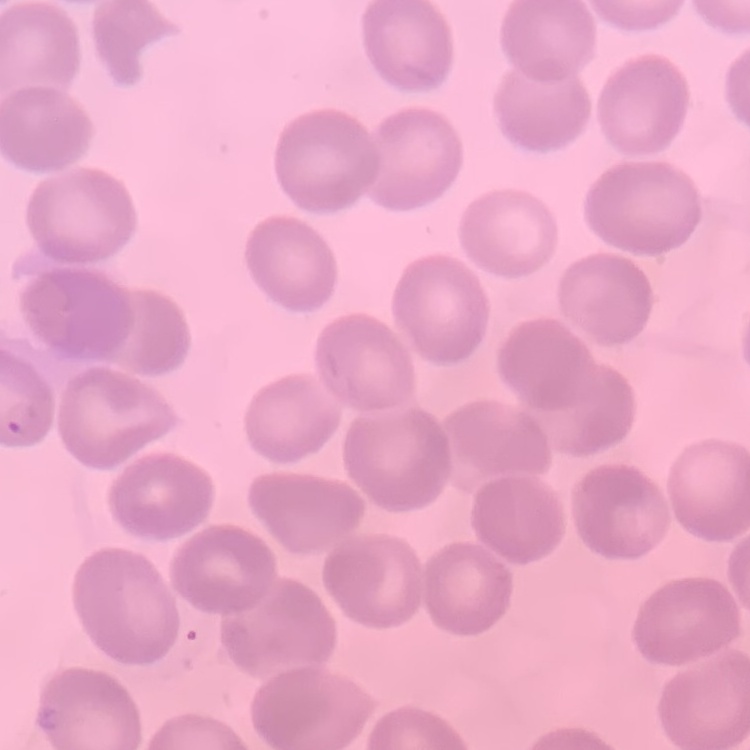

The erythrocytes show no rouleaux formation. Field's or Giemsa stain. One tile cut from a larger photomicrograph. Thin blood smear.